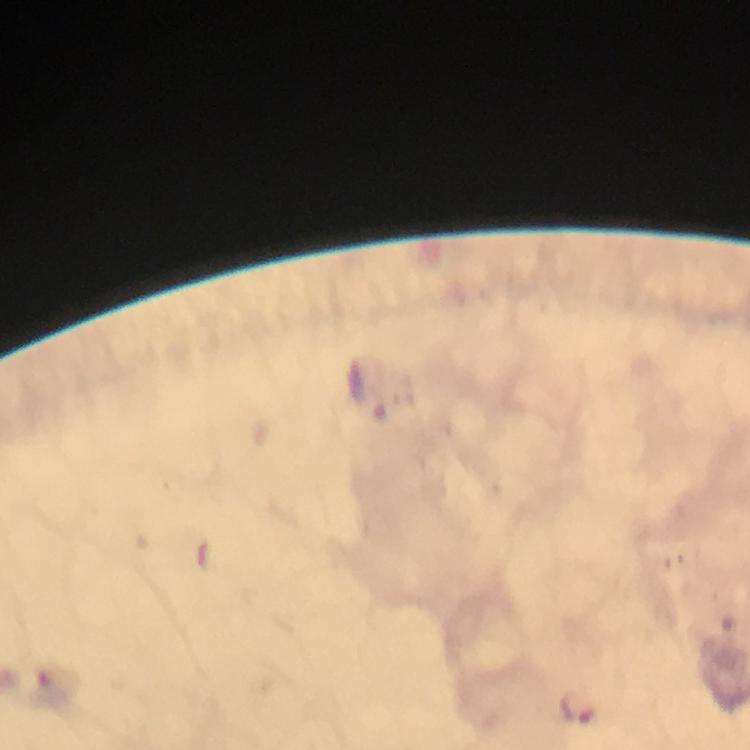

Approximate centers as (x, y) in pixels. Plasmodium parasite locations: (576, 707). Giemsa stain. Thick blood film. From a diagnostic examination for malaria. At 100x magnification. Immersion oil was used. A crop from one field of view. Image is 750×750 pixels. Smartphone photograph taken through a microscope.